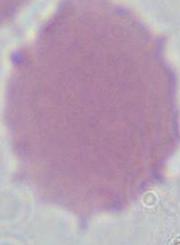
Summary:
  - Magnification: 1000x
  - Modality: photomicrograph
  - Identification: red blood cell